Name the parasite shown.
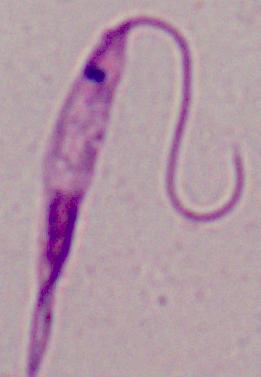
Leishmania.

modality = photomicrograph
magnification = 1000x